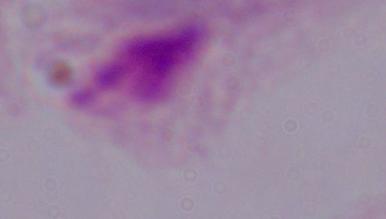

{
  "magnification": "1000x",
  "modality": "photomicrograph",
  "identification": "trichomonad"
}